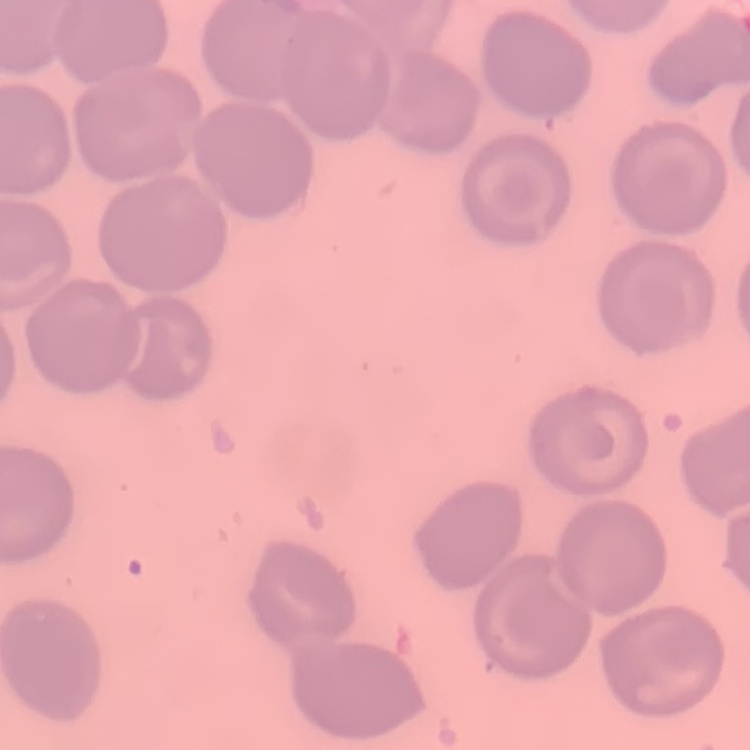

red blood cell morphology = no rouleaux formation
preparation = thin blood smear
stain = Field's or Giemsa
image type = square crop of a larger photomicrograph